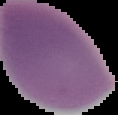
Image is 118×115 pixels. Segmented cell region on a black background. Result: negative for Plasmodium parasites. From a thin blood film.